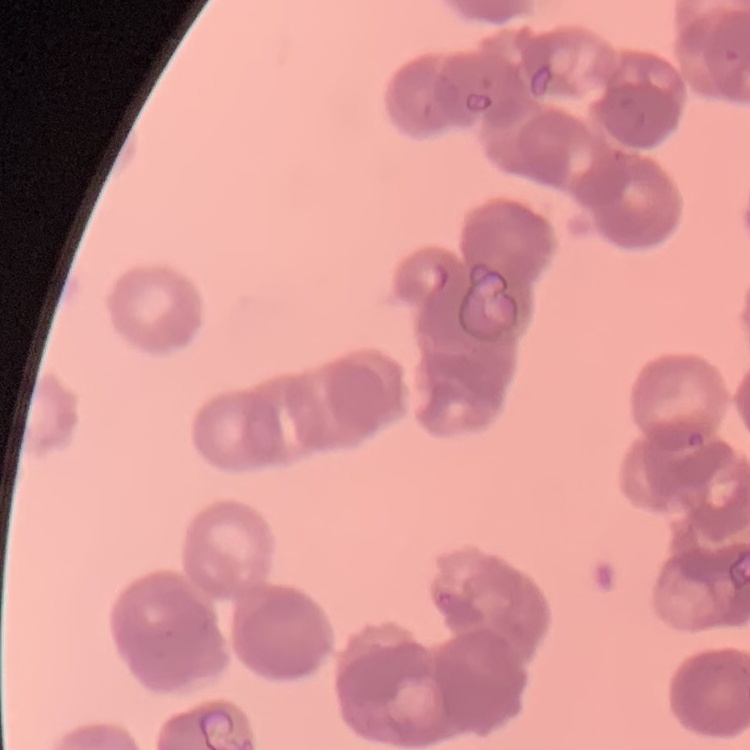
Summary:
  - Red blood cell morphology: rouleaux formation
  - Stain: Field's or Giemsa
  - Image type: one tile cut from a larger photomicrograph
  - Preparation: thin peripheral smear